Give the position of every Plasmodium parasite.
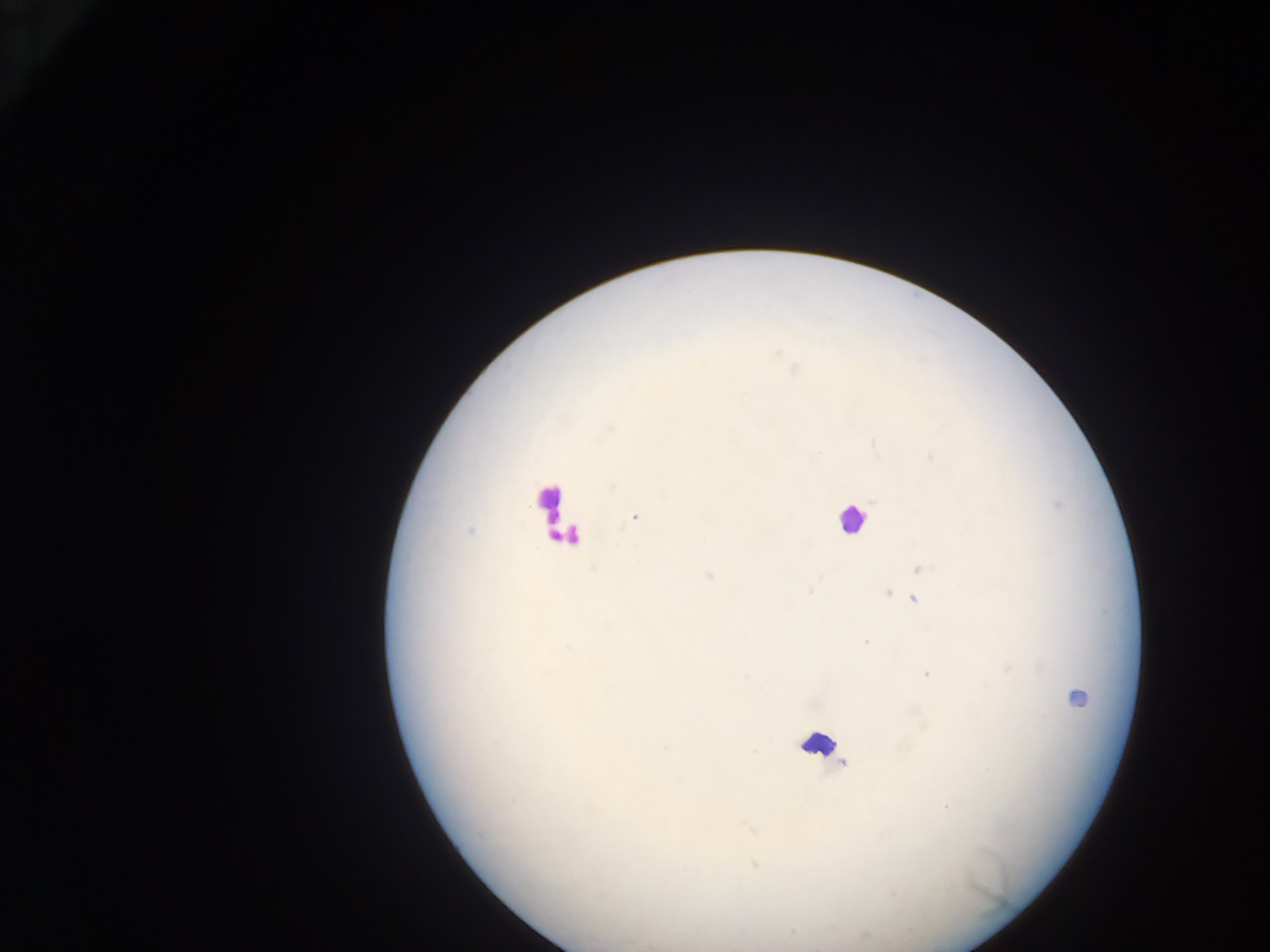
Approximate centers as (x, y) in pixels.
Plasmodium parasites: (634, 517), (919, 567), (708, 575), (886, 591), (913, 598), (865, 642), (927, 674), (1077, 698), (843, 763), (945, 804), (754, 866).

field of view = single
preparation = thick blood film
leukocyte locations = approximate centers as (x, y) in pixels: (552, 510), (851, 519), (565, 534), (817, 743)
capture = mobile-phone photograph through a microscope
country = Ghana
image size = 1270×952 pixels